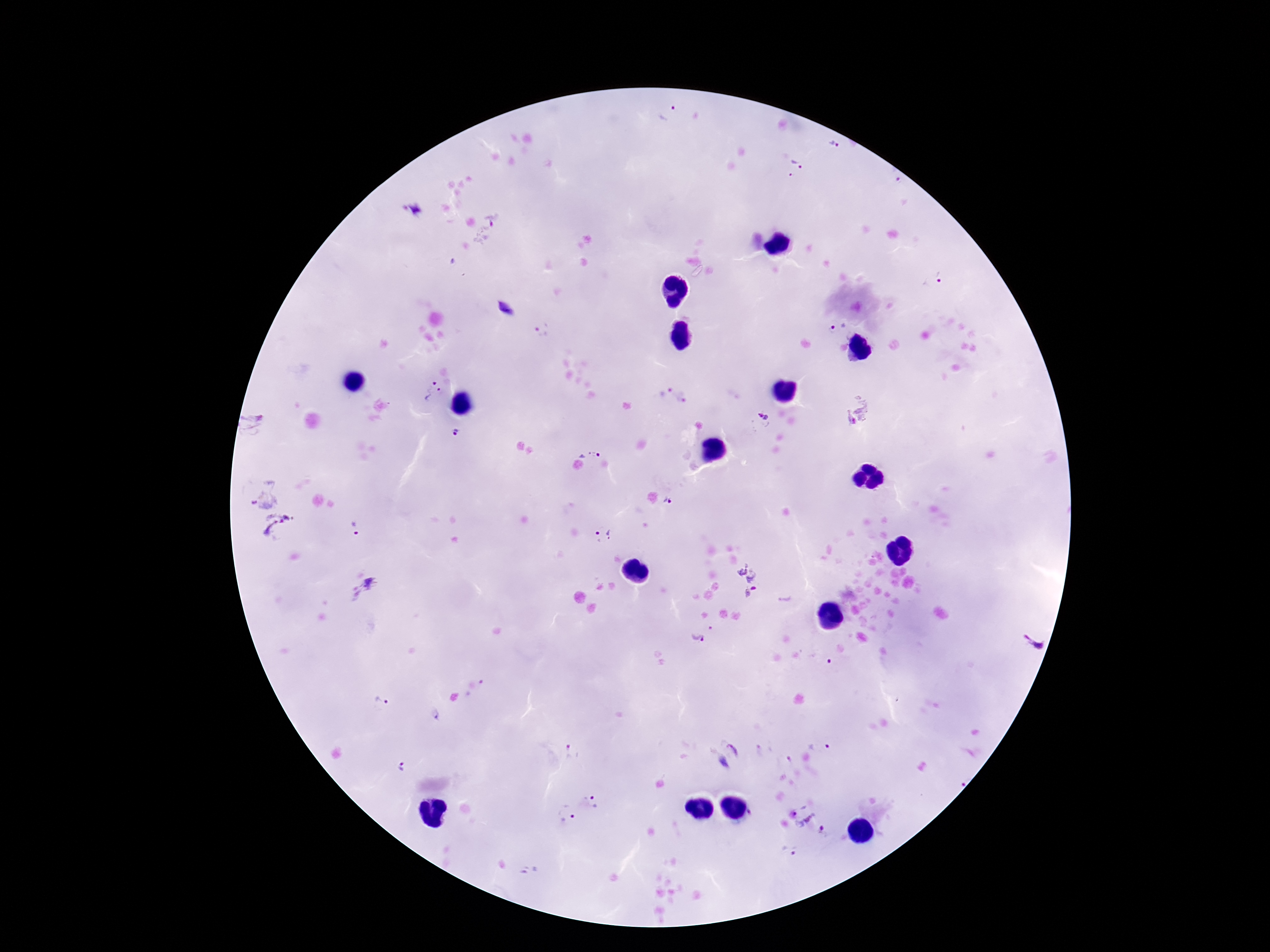

{
  "magnification": "100x",
  "stain": "Giemsa",
  "plasmodium_parasite_locations": "approximate centers as [x, y] in pixels: [669, 116], [832, 143], [798, 164], [894, 175], [412, 209], [494, 218], [932, 282], [506, 309], [838, 327], [542, 331], [663, 389], [432, 390], [682, 397], [857, 408], [762, 420], [257, 423], [455, 434], [591, 445], [261, 492], [673, 500], [280, 528], [356, 530], [603, 535], [745, 581], [364, 591], [697, 635], [1032, 646], [380, 703], [436, 716], [736, 747], [819, 747], [570, 753], [400, 767], [596, 802], [804, 808], [567, 815], [826, 831], [789, 851]",
  "image_size": "1270×952 pixels",
  "capture": "smartphone camera through the microscope eyepiece",
  "preparation": "thick blood film",
  "field_of_view": "one from this slide",
  "patient_malaria_status": "positive"
}